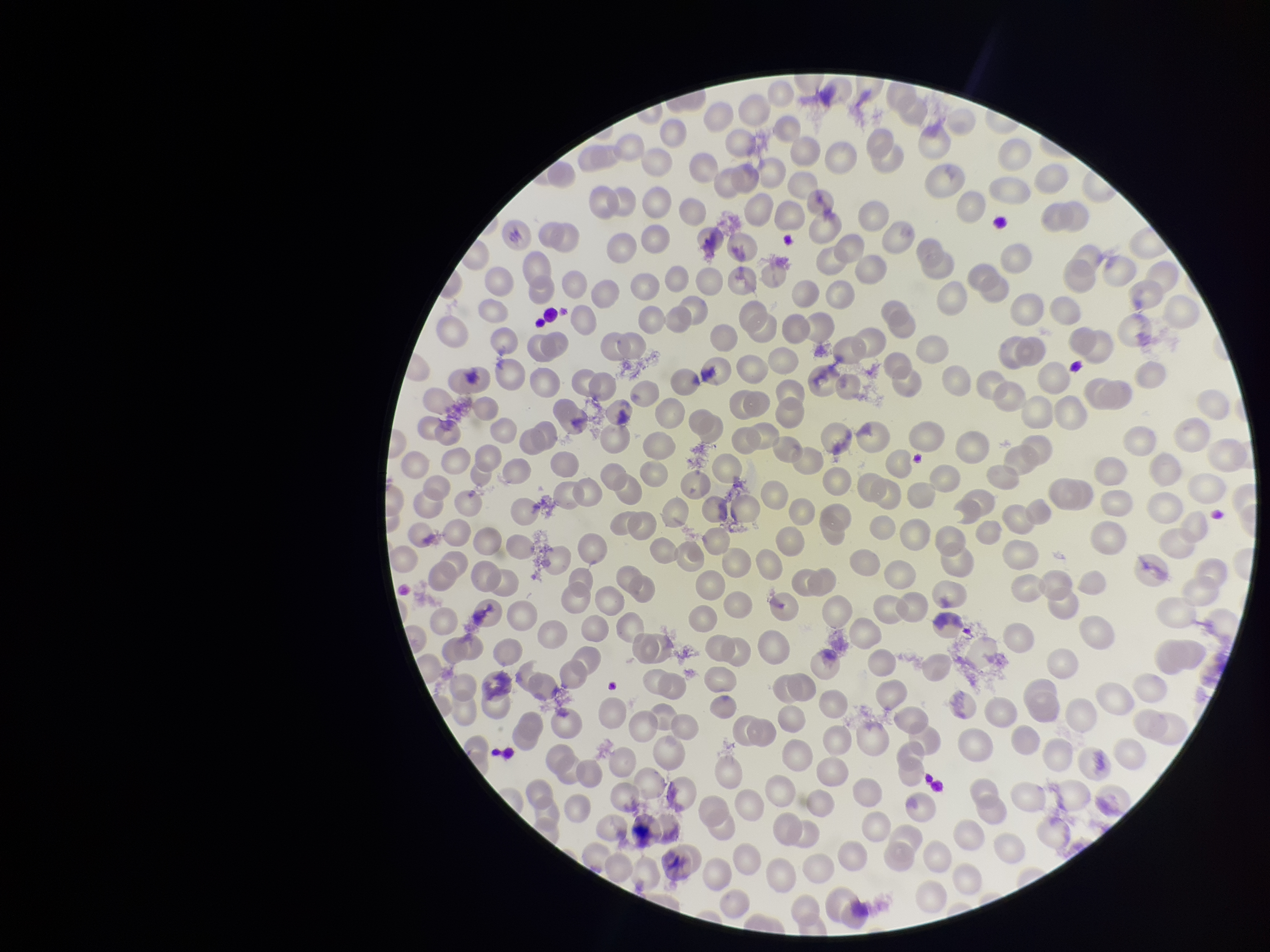

Summary:
  - Capture: smartphone photograph through the microscope eyepiece
  - Species reported for this patient: Plasmodium vivax
  - Parasitized red blood cells: none detected
  - Preparation: thin smear
  - Image size: 1270×952 pixels
  - Red blood cell count: 260
  - Parasitized red blood cell count: 0
  - Patient malaria status: infected
  - Stain: Giemsa
  - Field of view: one from this slide